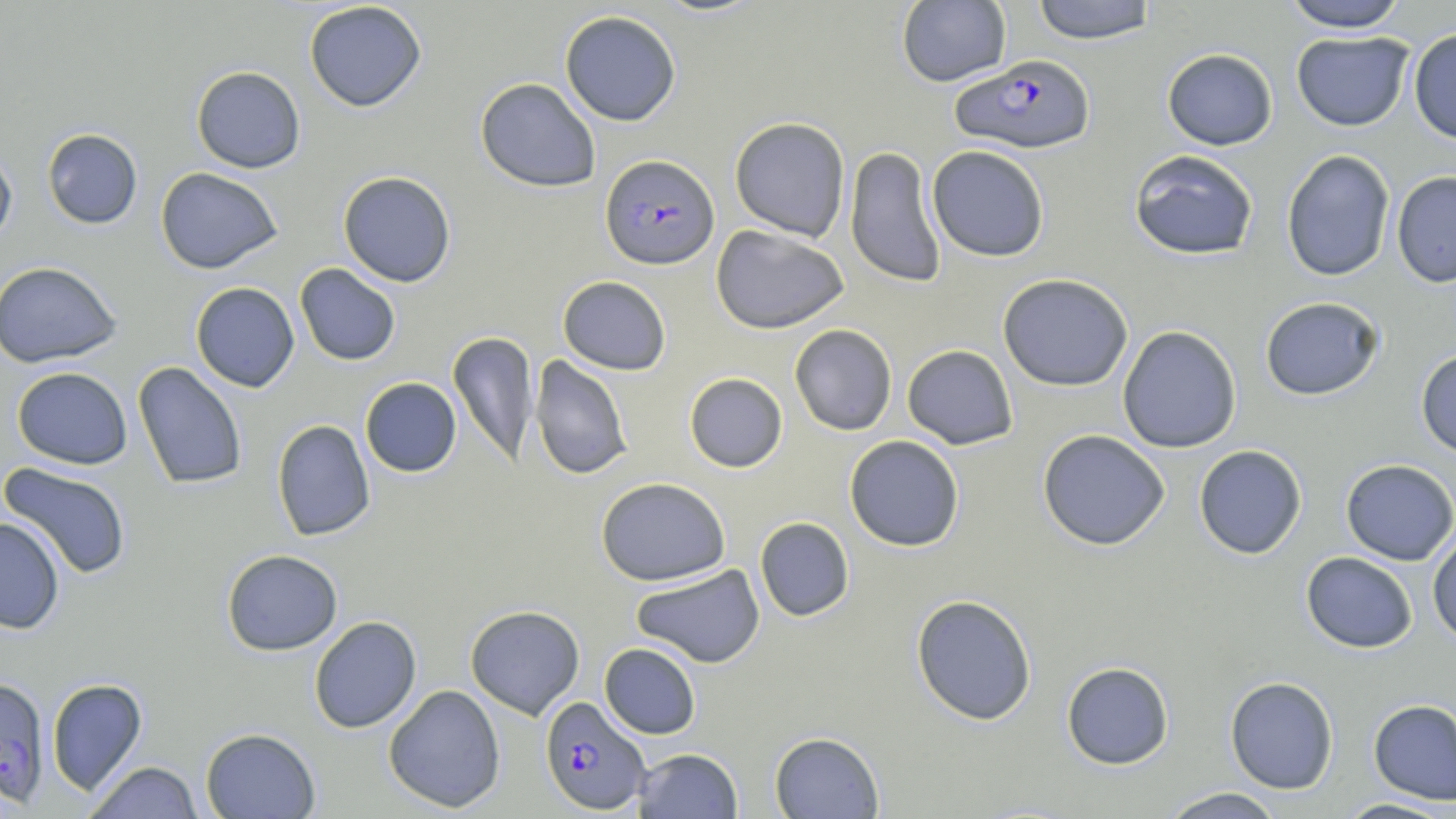
slide-level diagnosis = Plasmodium falciparum
magnification = 1000x
modality = light microscopy
Plasmodium falciparum-infected red blood cell locations = approximate bounding boxes as (x1, y1, x2, y2) in pixels: (951, 54, 1096, 153), (600, 154, 720, 270), (0, 675, 51, 808), (540, 696, 650, 814)
image size = 1456×819 pixels
preparation = thin blood smear
field of view = one of a larger specimen
uninfected red blood cell locations = approximate bounding boxes as (x1, y1, x2, y2) in pixels: (896, 0, 1011, 87), (304, 1, 427, 112), (1030, 1, 1158, 44), (1281, 1, 1409, 32), (559, 10, 681, 126), (1408, 28, 1456, 144), (1291, 31, 1414, 132), (1162, 48, 1278, 150), (191, 66, 306, 173), (475, 77, 601, 192), (730, 116, 850, 241), (42, 128, 143, 229), (844, 145, 947, 288), (927, 145, 1050, 262), (0, 146, 17, 249), (1128, 149, 1260, 260), (1281, 149, 1396, 282), (156, 167, 283, 274), (1391, 170, 1456, 288), (338, 171, 456, 287), (711, 224, 849, 334), (0, 261, 122, 368), (295, 263, 401, 365), (997, 273, 1133, 391), (557, 275, 671, 375), (191, 282, 300, 392), (1260, 296, 1384, 400), (789, 324, 897, 436), (1117, 325, 1242, 453), (448, 331, 538, 468), (902, 344, 1018, 449), (1415, 348, 1456, 459), (529, 354, 634, 481), (132, 361, 248, 490), (12, 366, 133, 470), (684, 372, 788, 472), (360, 377, 462, 477), (271, 419, 376, 541), (1037, 429, 1170, 551), (844, 435, 965, 552), (1193, 445, 1307, 559), (1340, 459, 1456, 565), (0, 462, 133, 580), (596, 477, 730, 586), (0, 516, 65, 634), (754, 517, 855, 621), (1427, 529, 1456, 646), (221, 549, 343, 655), (1301, 552, 1418, 653), (630, 564, 765, 669), (911, 594, 1037, 725), (465, 605, 585, 719), (309, 615, 422, 733), (599, 643, 701, 739), (1061, 661, 1174, 770), (1224, 676, 1339, 794), (46, 678, 148, 795), (383, 684, 506, 813), (1368, 698, 1456, 806), (200, 727, 321, 818), (770, 731, 885, 818), (633, 748, 743, 818), (84, 761, 203, 818), (1158, 787, 1286, 818), (1333, 797, 1455, 818)
stain = May-Grünwald-Giemsa